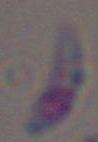

{
  "magnification": "1000x",
  "identification": "Toxoplasma gondii",
  "modality": "photomicrograph"
}